Outline each uninfected red blood cell.
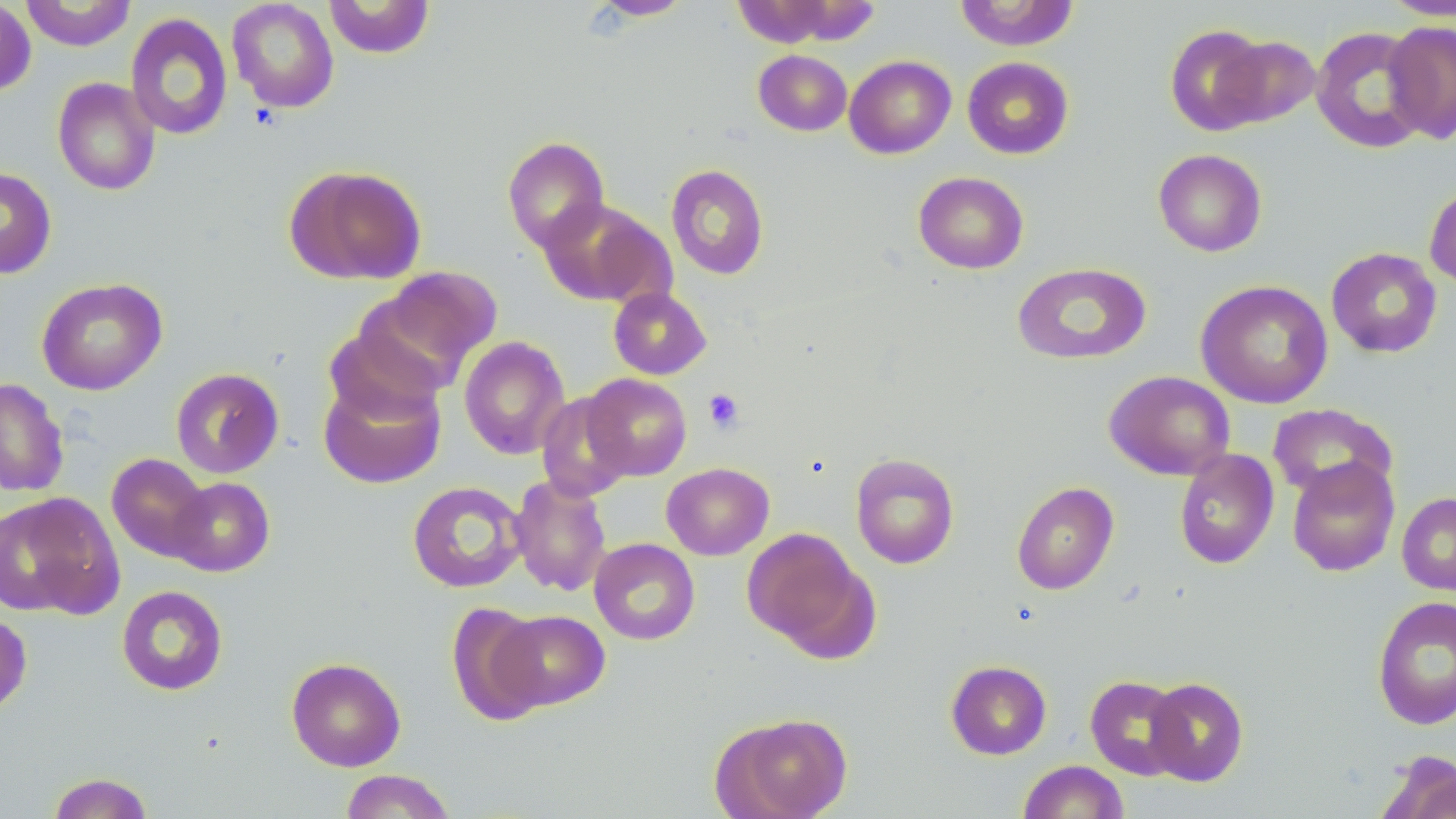
Approximate bounding boxes as (x1,y1)-(x2,y2) corner pairs in pixels.
Uninfected red blood cells: (19,0)-(137,51), (226,0)-(340,113), (324,0)-(435,59), (587,0)-(694,20), (731,0)-(840,48), (1379,0)-(1456,20), (0,1)-(37,96), (953,1)-(1080,51), (125,12)-(233,140), (1382,20)-(1456,145), (1164,23)-(1272,136), (1310,26)-(1431,154), (1215,34)-(1321,129), (753,49)-(852,136), (844,55)-(956,159), (962,56)-(1074,159), (52,77)-(161,196), (502,136)-(610,252), (1153,148)-(1267,256), (284,164)-(428,285), (665,164)-(769,280), (0,167)-(57,279), (914,171)-(1029,273), (1424,181)-(1456,290), (537,198)-(666,307), (1326,247)-(1442,358), (1012,262)-(1151,364), (369,266)-(503,381), (36,277)-(167,395), (1195,280)-(1333,408), (608,286)-(712,380), (459,336)-(570,460), (170,367)-(285,479), (1104,370)-(1235,480), (318,371)-(447,490), (581,373)-(692,480), (0,377)-(70,497), (536,393)-(635,502), (1267,403)-(1398,503), (1174,449)-(1279,570), (106,453)-(212,562), (850,453)-(960,569), (1287,456)-(1400,576), (662,462)-(774,560), (509,475)-(612,596), (168,476)-(275,577), (407,480)-(528,593), (1011,481)-(1119,594), (1397,492)-(1456,595), (0,493)-(123,619), (741,528)-(872,654), (589,538)-(700,645), (116,585)-(229,696), (1372,595)-(1456,730), (446,601)-(550,725), (493,610)-(610,711), (0,612)-(32,716), (286,656)-(406,771), (945,660)-(1052,760), (1084,675)-(1189,780), (1144,677)-(1249,786), (712,711)-(853,819), (1374,750)-(1456,819), (1017,760)-(1129,819), (339,769)-(456,818), (46,772)-(155,818).

slide-level diagnosis = negative for blood parasites
stain = May-Grünwald-Giemsa
modality = optical microscopy
field of view = single
preparation = thin blood smear
platelet locations = approximate bounding boxes as (x1,y1)-(x2,y2) corner pairs in pixels: (703,388)-(745,434)
magnification = 1000x
image size = 1456×819 pixels